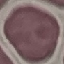

Malaria status: uninfected. Giemsa-stained preparation. Thin blood smear. Automatically extracted cell patch, resized to 64 × 64 pixels. Photographed with a smartphone camera at the microscope eyepiece.